State the blood parasite species.
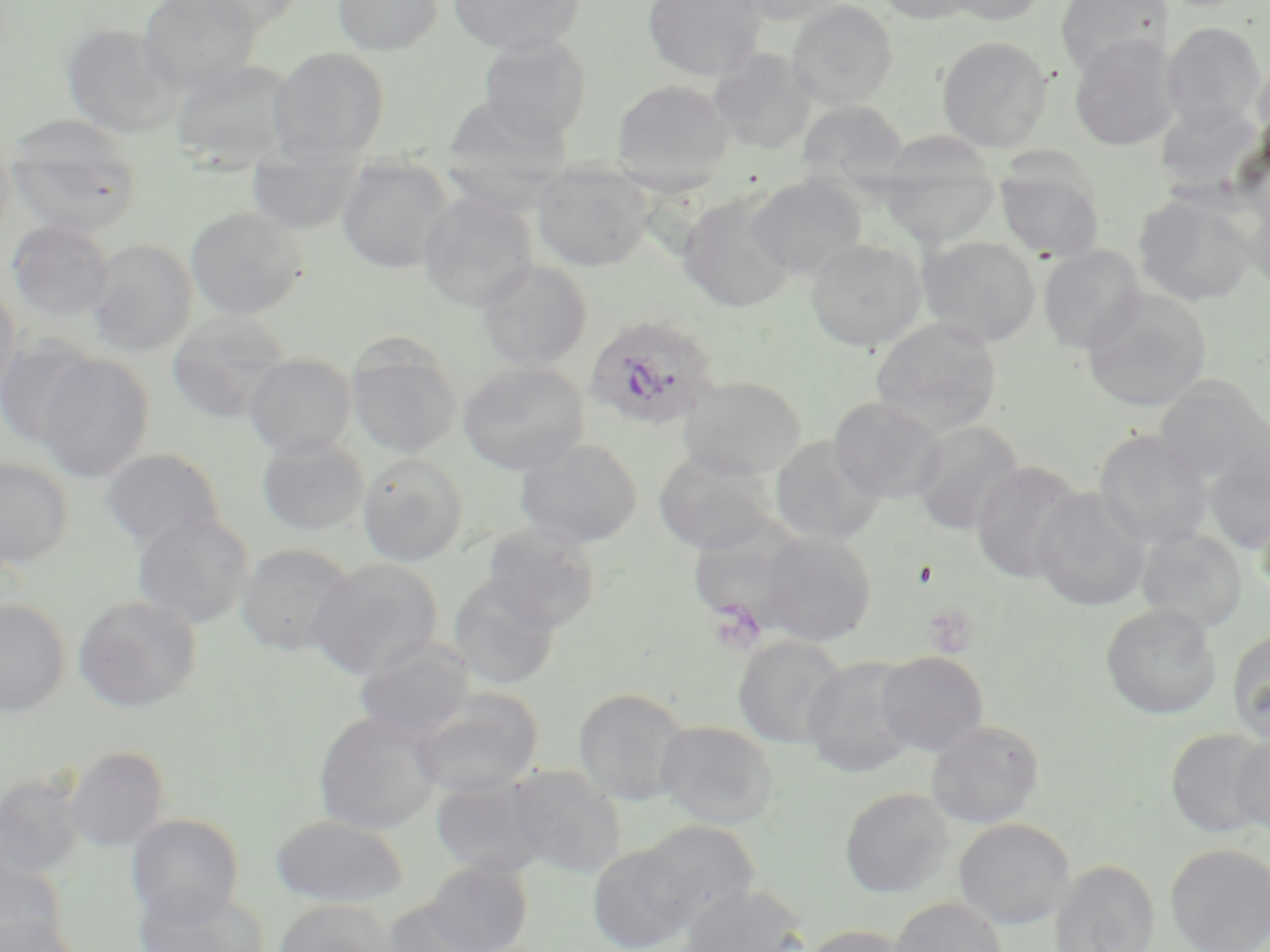

Plasmodium ovale.

Summary:
  - Coordinate format: approximate bounding boxes as (x1,y1)-(x2,y2) corner pairs in pixels
  - Plasmodium ovale-infected red blood cell locations: (582,313)-(723,433)
  - Platelet locations (subset): (707,599)-(766,653)
  - Uninfected red blood cell locations (subset): (138,0)-(263,94), (185,0)-(309,32), (332,0)-(443,56), (448,0)-(585,54), (642,0)-(767,81), (733,0)-(850,26), (786,0)-(898,110), (873,0)-(981,25), (939,0)-(1049,26), (1054,0)-(1173,78), (1162,22)-(1267,132), (61,23)-(180,138), (476,33)-(592,144), (1068,33)-(1180,153), (937,36)-(1053,152), (266,47)-(391,164), (708,48)-(815,154), (1252,53)-(1270,163), (169,58)-(296,173), (611,79)-(736,193), (796,100)-(908,189), (1155,101)-(1267,197), (5,118)-(143,237), (0,132)-(16,248), (878,136)-(1002,247), (246,147)-(364,234), (336,156)-(456,274), (994,156)-(1105,262), (533,162)-(654,271), (747,174)-(867,280), (418,191)-(539,311), (678,191)-(798,312), (1133,191)-(1258,307), (1244,192)-(1270,294), (185,206)-(306,320), (7,220)-(115,320), (918,236)-(1041,346), (805,238)-(926,350), (88,239)-(198,356), (1038,245)-(1146,353), (477,259)-(593,371), (0,284)-(23,404), (1081,290)-(1212,412), (166,312)-(291,425), (871,316)-(1003,434), (0,336)-(99,447), (346,336)-(462,458), (244,353)-(357,459), (36,354)-(155,482), (457,361)-(590,474), (678,375)-(807,481), (1153,379)-(1269,486), (829,396)-(947,503), (909,420)-(1025,537), (1094,429)-(1214,550), (770,435)-(885,545), (256,436)-(370,536), (515,437)-(643,547), (1203,445)-(1270,554), (100,448)-(226,549), (653,450)-(776,555), (357,454)-(469,566), (0,458)-(73,569), (971,461)-(1085,583), (1033,488)-(1151,612), (1255,501)-(1270,602), (131,513)-(254,629), (481,521)-(602,633), (1136,529)-(1248,631), (758,530)-(877,646), (236,542)-(357,657), (309,558)-(443,679), (447,576)-(561,690), (73,595)-(203,713), (0,598)-(70,718), (1100,603)-(1221,719), (1226,629)-(1270,744), (732,635)-(848,748), (353,638)-(475,742), (875,650)-(989,755), (803,655)-(920,777), (409,687)-(543,797), (573,687)-(693,805), (313,710)-(444,835), (925,719)-(1045,828), (655,720)-(780,829), (1166,728)-(1269,838), (1231,732)-(1270,838), (65,746)-(171,853), (504,763)-(628,878), (0,773)-(86,877), (430,776)-(552,878), (839,787)-(955,898), (126,813)-(244,926), (270,814)-(409,908), (954,818)-(1074,929), (636,820)-(760,926), (0,841)-(69,945), (587,843)-(700,952), (1165,843)-(1270,952), (422,860)-(533,952), (1050,860)-(1159,952), (680,885)-(810,951), (134,886)-(271,951), (889,896)-(1008,952), (274,899)-(396,952), (380,899)-(494,951), (0,915)-(80,952), (798,924)-(913,952)
  - Field of view: one of a larger specimen
  - Stain: May-Grünwald-Giemsa
  - Magnification: 1000x
  - Preparation: thin blood film
  - Image size: 1270×952 pixels
  - Modality: optical microscopy